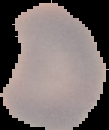
Summary:
  - Preparation: thin blood film
  - Image size: 109×130 pixels
  - Malaria status: uninfected
  - Image type: segmented cell region with the area outside set to black